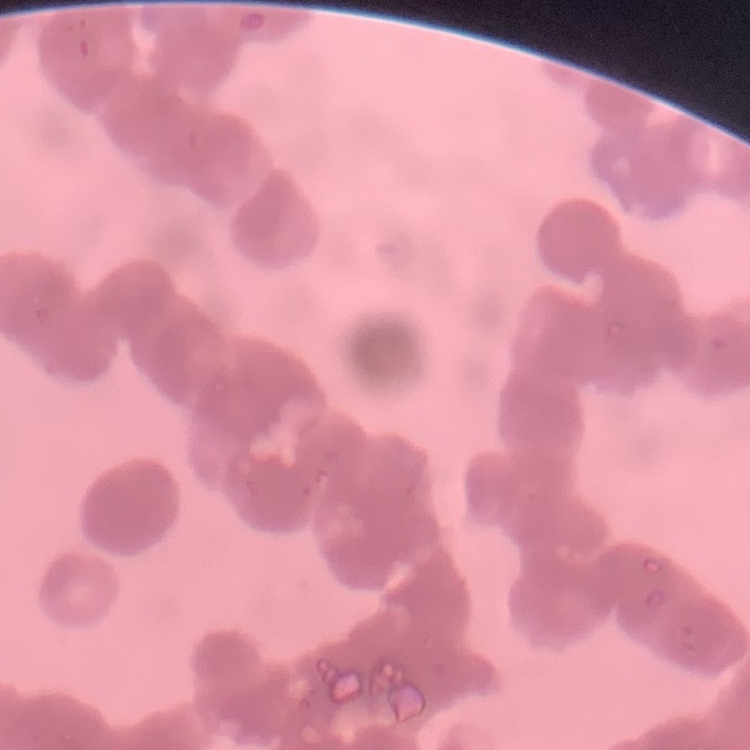
erythrocyte morphology = rouleaux formation
stain = Field's or Giemsa
image type = one tile cut from a larger photomicrograph
preparation = thin peripheral smear